Name the cell type shown.
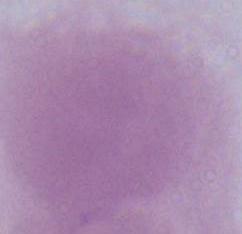
An erythrocyte.

Summary:
  - Magnification: 1000x
  - Modality: micrograph